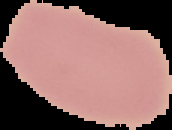 From a thin blood smear. Segmented cell region on a black background. Result: no Plasmodium parasites detected. Image is 172×130 pixels.